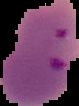
{
  "image_type": "segmented cell region with the area outside set to black",
  "image_size": "79×106 pixels",
  "preparation": "thin blood film",
  "result": "malaria parasites identified"
}